Name the parasite shown.
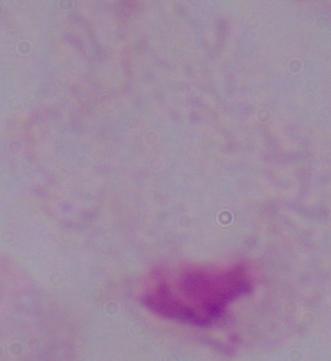
A trichomonad.

magnification = 1000x
modality = micrograph